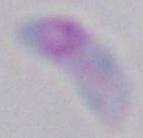

Summary:
  - Magnification: 1000x
  - Modality: micrograph
  - Identification: Toxoplasma gondii